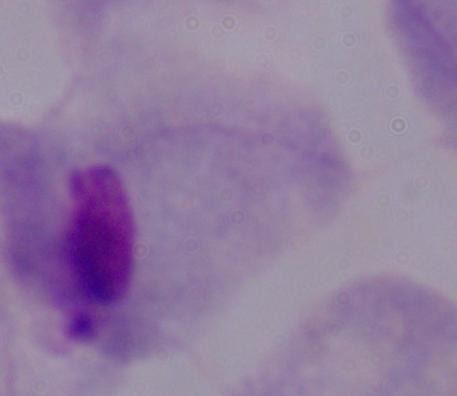

Summary:
  - Magnification: 1000x
  - Identification: trichomonad
  - Modality: photomicrograph